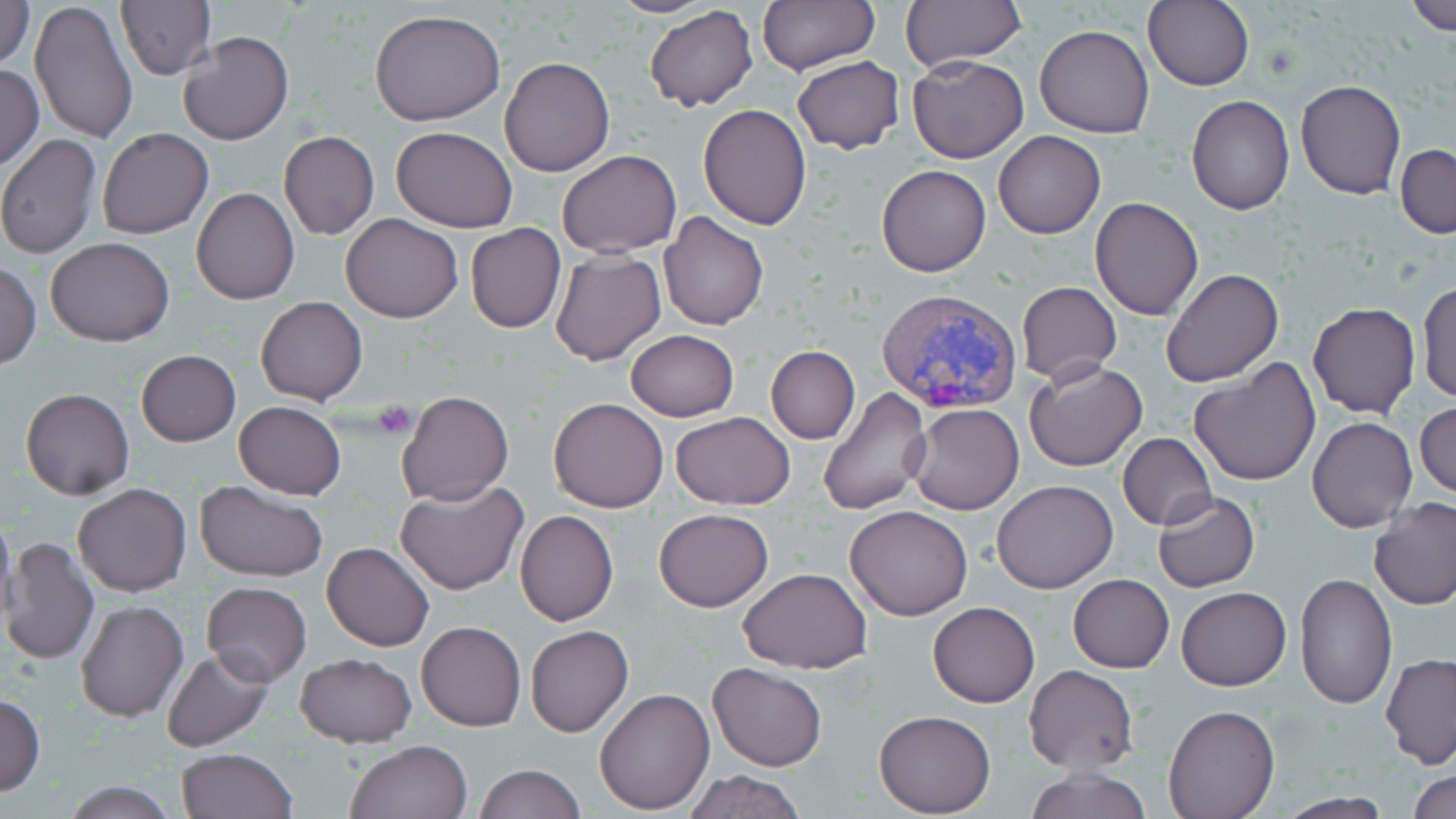
Summary:
  - Coordinate format: approximate bounding boxes as [x1, y1, x2, y2] in pixels
  - Platelet locations: [372, 401, 417, 439]
  - Uninfected red blood cell locations: [0, 0, 36, 68], [30, 0, 136, 146], [605, 0, 718, 17], [757, 0, 878, 75], [901, 0, 1023, 70], [1142, 0, 1256, 91], [1405, 0, 1456, 35], [115, 1, 214, 81], [643, 5, 760, 111], [368, 8, 505, 125], [1035, 25, 1153, 139], [177, 30, 293, 145], [907, 54, 1030, 163], [499, 57, 615, 176], [791, 57, 904, 152], [0, 64, 44, 172], [1295, 80, 1405, 199], [1186, 94, 1295, 214], [698, 104, 811, 230], [391, 126, 518, 232], [96, 128, 213, 239], [993, 130, 1106, 238], [279, 132, 380, 240], [0, 133, 101, 258], [1395, 143, 1456, 238], [556, 149, 682, 258], [876, 165, 991, 276], [191, 187, 301, 305], [1090, 198, 1204, 320], [659, 212, 769, 329], [342, 213, 463, 323], [465, 223, 565, 332], [46, 237, 175, 347], [550, 249, 666, 367], [1, 262, 41, 369], [1160, 267, 1284, 388], [1417, 281, 1456, 405], [1017, 282, 1121, 385], [256, 297, 367, 405], [1306, 302, 1420, 418], [624, 330, 739, 422], [766, 345, 860, 444], [135, 350, 240, 447], [1189, 355, 1321, 487], [1023, 358, 1148, 472], [817, 386, 931, 518], [20, 388, 134, 500], [399, 391, 513, 506], [548, 397, 670, 513], [233, 401, 348, 499], [1414, 402, 1455, 500], [907, 404, 1024, 515], [670, 412, 796, 508], [1308, 417, 1416, 532], [1118, 433, 1216, 530], [194, 479, 329, 582], [395, 479, 529, 596], [992, 479, 1118, 593], [73, 482, 192, 598], [1152, 491, 1259, 592], [1369, 497, 1456, 609], [845, 503, 974, 620], [653, 508, 774, 611], [515, 510, 619, 627], [0, 511, 17, 631], [0, 534, 100, 667], [321, 540, 435, 651], [739, 567, 872, 674], [1294, 573, 1397, 709], [1068, 574, 1174, 673], [202, 581, 312, 686], [1178, 586, 1290, 691], [76, 599, 188, 723], [928, 602, 1039, 707], [416, 622, 525, 731], [526, 625, 633, 736], [162, 648, 274, 752], [294, 652, 416, 746], [1381, 653, 1456, 767], [708, 662, 827, 770], [1023, 664, 1138, 774], [593, 686, 714, 813], [0, 692, 45, 797], [1162, 704, 1279, 818], [873, 710, 995, 817], [345, 739, 473, 819], [176, 749, 296, 819], [474, 763, 585, 819], [1025, 766, 1151, 819], [685, 768, 807, 819], [1409, 768, 1456, 819], [60, 781, 179, 817], [1275, 794, 1395, 819]
  - Plasmodium vivax-infected red blood cell locations: [875, 287, 1022, 415]
  - Slide-level diagnosis: Plasmodium vivax
  - Modality: optical microscopy
  - Preparation: thin blood smear
  - Stain: May-Grünwald-Giemsa
  - Image size: 1456×819 pixels
  - Magnification: 1000x
  - Field of view: single